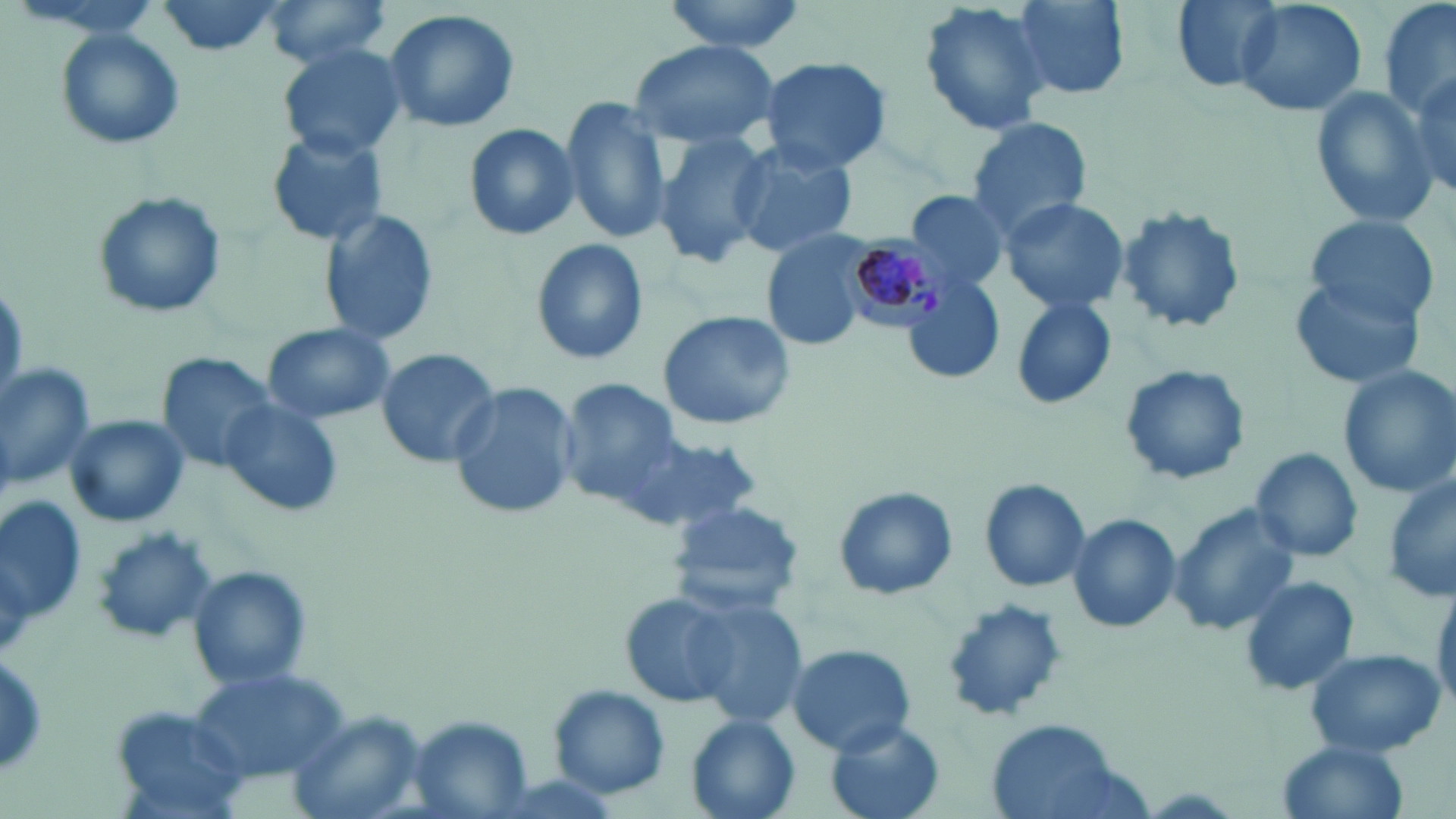

Summary:
  - Coordinate format: approximate bounding boxes as [x1, y1, x2, y2] in pixels
  - Plasmodium malariae-infected red blood cell locations: [838, 230, 958, 333]
  - Uninfected red blood cell locations: [149, 0, 291, 57], [256, 0, 397, 69], [657, 0, 809, 53], [1010, 0, 1131, 99], [1169, 0, 1282, 93], [1235, 0, 1365, 117], [1380, 0, 1454, 123], [917, 1, 1054, 139], [384, 8, 521, 135], [56, 30, 185, 151], [627, 38, 779, 150], [277, 43, 407, 160], [759, 55, 894, 173], [1405, 63, 1454, 204], [1309, 85, 1442, 227], [559, 95, 675, 245], [963, 116, 1093, 244], [462, 123, 580, 242], [653, 128, 774, 269], [264, 130, 390, 247], [729, 140, 859, 259], [907, 189, 1011, 296], [90, 190, 229, 323], [999, 196, 1129, 314], [1113, 205, 1247, 336], [317, 207, 441, 349], [1305, 218, 1439, 322], [760, 229, 878, 351], [528, 237, 649, 366], [1290, 272, 1428, 389], [902, 278, 1007, 385], [1008, 296, 1118, 412], [657, 311, 798, 431], [261, 324, 395, 424], [374, 348, 503, 468], [156, 356, 287, 473], [0, 361, 95, 493], [1119, 363, 1250, 487], [1336, 363, 1456, 499], [558, 378, 686, 507], [446, 380, 579, 521], [221, 398, 339, 517], [65, 415, 191, 527], [615, 433, 758, 534], [1248, 445, 1364, 564], [1382, 474, 1456, 607], [979, 476, 1093, 594], [833, 485, 958, 602], [1, 497, 88, 634], [666, 499, 805, 617], [1167, 499, 1303, 637], [1065, 511, 1180, 636], [90, 526, 220, 646], [187, 566, 313, 692], [1239, 574, 1360, 698], [1430, 578, 1456, 714], [616, 588, 746, 711], [686, 595, 811, 732], [939, 599, 1069, 725], [786, 643, 917, 756], [1303, 646, 1444, 758], [184, 665, 352, 789], [548, 685, 672, 800], [284, 711, 424, 819], [685, 716, 802, 819], [403, 717, 538, 819], [985, 717, 1132, 819], [823, 718, 949, 819], [1275, 740, 1412, 819]
  - Slide-level diagnosis: Plasmodium malariae
  - Field of view: single
  - Modality: light microscopy
  - Magnification: 1000x
  - Stain: May-Grünwald-Giemsa
  - Image size: 1456×819 pixels
  - Preparation: thin blood film